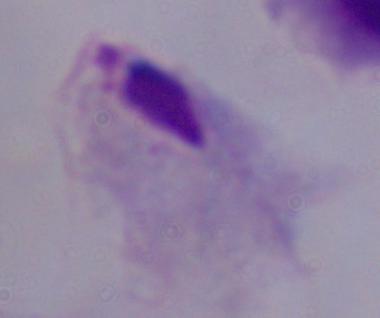 A trichomonad is seen. 1000x magnification. Photomicrograph.